Outline each white blood cell.
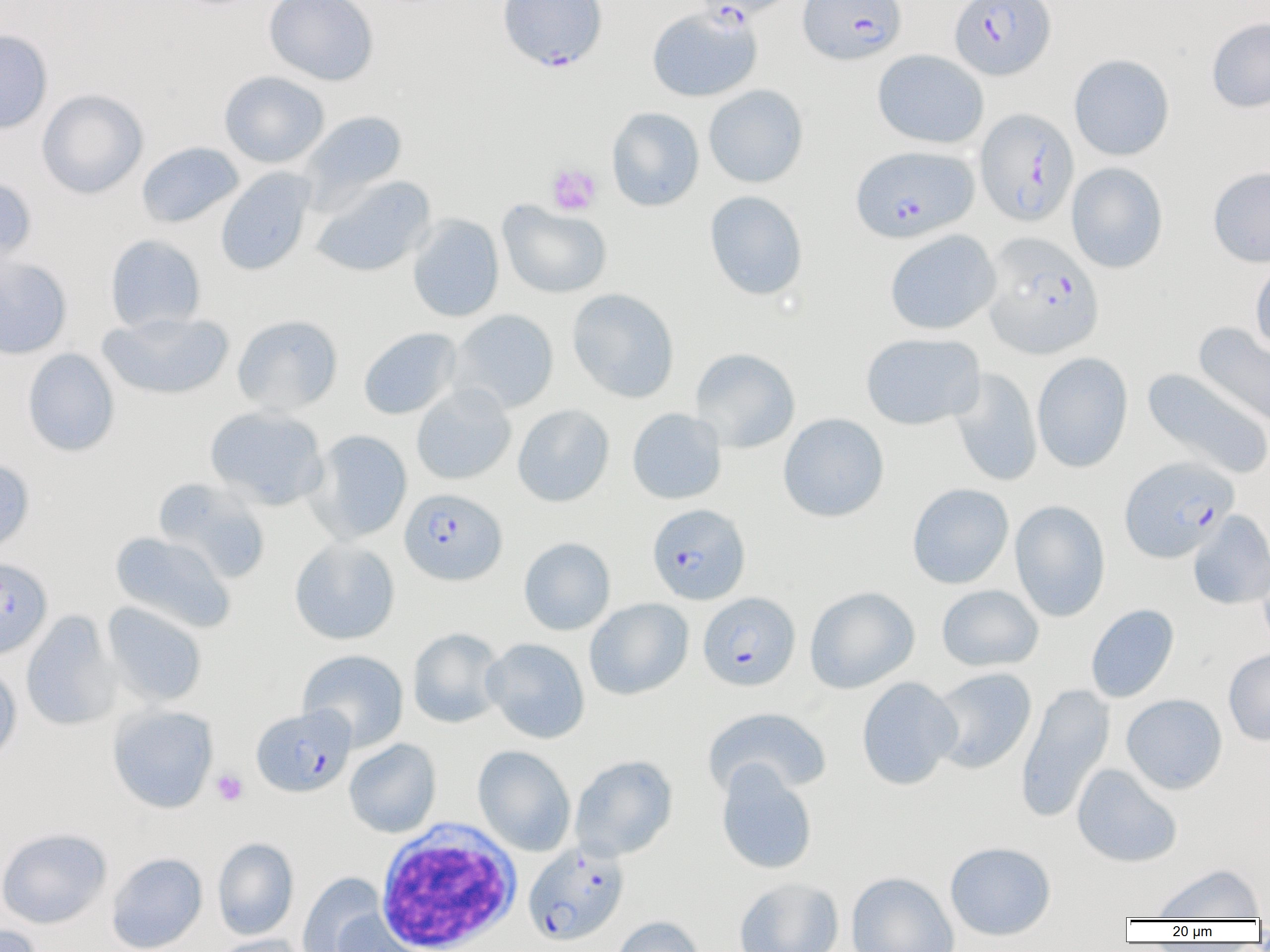

Approximate bounding boxes as (x1,y1)-(x2,y2) corner pairs in pixels.
White blood cells: (374,819)-(523,952).

slide-level diagnosis = Plasmodium falciparum
modality = optical microscopy
field of view = single
preparation = thin blood film
platelet locations = approximate bounding boxes as (x1,y1)-(x2,y2) corner pairs in pixels: (546,164)-(601,216), (211,769)-(248,805)
uninfected red blood cell locations = approximate bounding boxes as (x1,y1)-(x2,y2) corner pairs in pixels: (264,0)-(379,85), (647,6)-(762,102), (1206,17)-(1270,113), (0,30)-(53,135), (872,49)-(989,149), (1069,53)-(1175,161), (219,71)-(330,168), (704,84)-(808,188), (37,89)-(148,199), (606,107)-(704,212), (301,110)-(407,206), (137,142)-(243,229), (1067,162)-(1168,273), (1208,166)-(1270,267), (215,168)-(315,276), (0,176)-(38,270), (310,176)-(435,278), (704,190)-(808,300), (498,200)-(612,299), (407,214)-(504,323), (884,230)-(1001,335), (105,234)-(206,332), (0,255)-(72,359), (1250,258)-(1270,355), (567,288)-(679,403), (97,310)-(235,401), (450,310)-(559,413), (232,314)-(343,415), (1193,322)-(1270,428), (358,327)-(461,420), (860,332)-(985,431), (690,347)-(800,453), (22,348)-(120,457), (1032,352)-(1133,473), (948,367)-(1043,487), (1141,368)-(1270,480), (411,384)-(516,485), (512,404)-(615,507), (205,406)-(329,510), (627,407)-(727,505), (778,413)-(889,522), (306,430)-(412,544), (0,456)-(35,558), (154,478)-(271,583), (907,483)-(1014,589), (1009,500)-(1111,622), (1187,510)-(1270,610), (110,531)-(236,634), (519,537)-(615,635), (289,538)-(401,645), (1258,560)-(1270,656), (936,585)-(1044,672), (804,586)-(920,694), (584,598)-(693,700), (102,602)-(208,708), (1085,604)-(1179,703), (21,610)-(121,731), (407,628)-(506,728), (482,638)-(590,744), (1223,648)-(1270,746), (297,649)-(409,752), (0,662)-(22,768), (929,667)-(1037,774), (856,677)-(961,790), (1015,682)-(1115,823), (1121,693)-(1228,794), (107,704)-(218,813), (702,707)-(832,799), (344,738)-(441,838), (472,745)-(576,856), (570,755)-(678,861), (716,762)-(818,875), (1071,764)-(1183,868), (0,827)-(112,929), (212,837)-(299,940), (944,841)-(1056,940), (106,852)-(208,952), (1149,863)-(1266,920), (298,872)-(388,952), (846,872)-(959,952), (734,877)-(844,952), (332,910)-(431,952), (609,915)-(706,952), (0,923)-(45,952), (209,934)-(310,952)
image size = 1270×952 pixels
magnification = 1000x
Plasmodium falciparum-infected red blood cell locations = approximate bounding boxes as (x1,y1)-(x2,y2) corner pairs in pixels: (497,0)-(608,71), (691,0)-(801,21), (799,0)-(906,65), (950,0)-(1056,80), (975,107)-(1079,226), (851,145)-(978,243), (982,232)-(1104,360), (1119,456)-(1239,562), (399,488)-(507,585), (647,503)-(750,605), (0,557)-(52,659), (698,592)-(800,691), (251,705)-(355,797), (523,841)-(629,946)